Name the parasite shown.
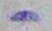

This is Toxoplasma gondii.

magnification = 1000x
modality = micrograph